Classify this cell by malaria status.
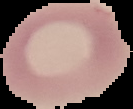
Uninfected.

From a thin blood film. Image is 133×109 pixels. Cell region segmented out of the field of view; the surrounding area is masked to black.